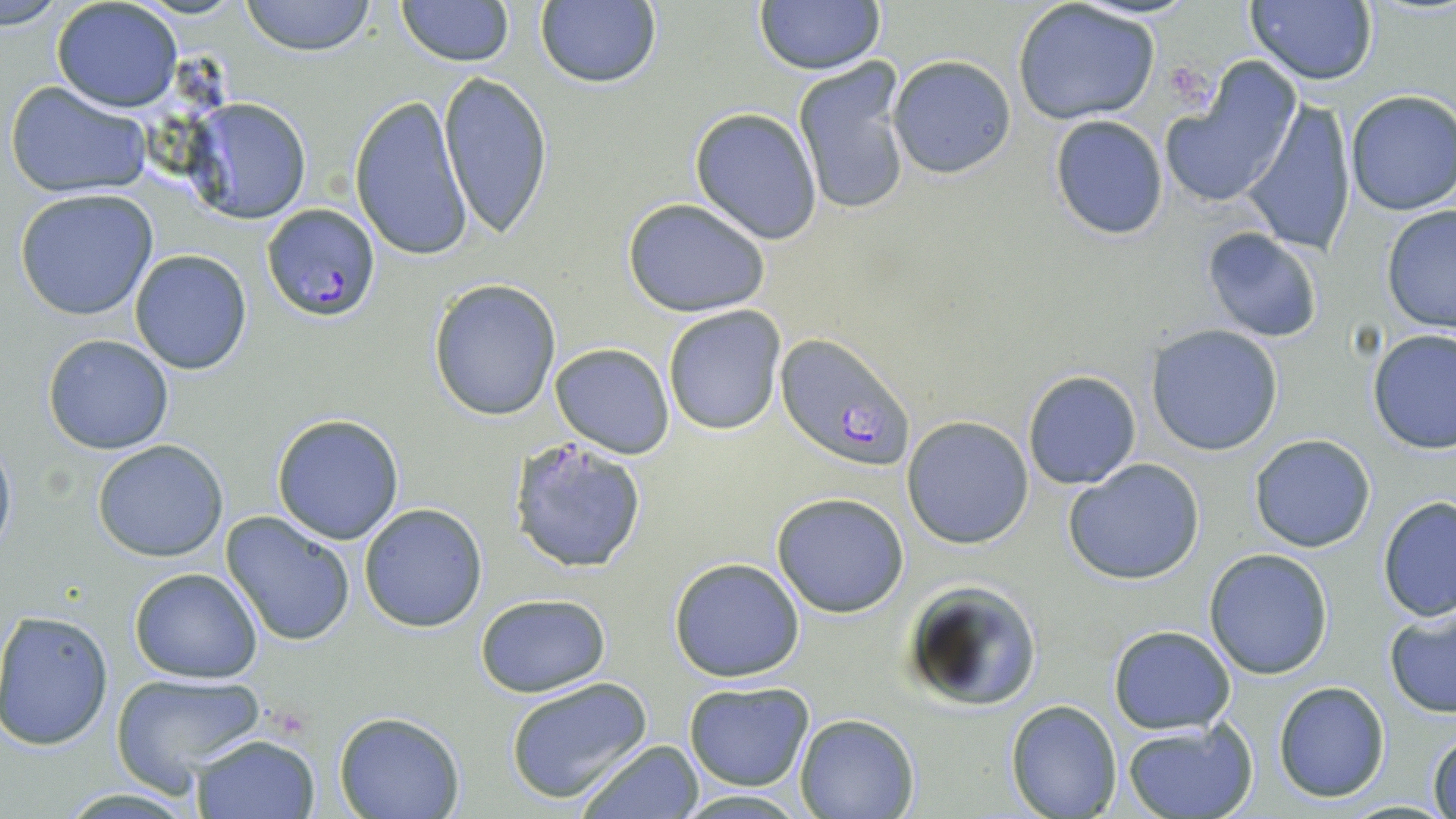

Approximate bounding boxes as (x1,y1)-(x2,y2) corner pairs in pixels. Plasmodium falciparum-infected red blood cell locations: (261,203)-(382,321), (775,335)-(915,474). Uninfected red blood cell locations: (239,0)-(379,56), (396,0)-(512,66), (3,1)-(61,29), (51,1)-(183,112), (534,1)-(663,89), (754,1)-(886,76), (1244,1)-(1380,89), (1013,2)-(1161,125), (887,54)-(1017,180), (792,60)-(911,217), (1160,68)-(1300,209), (438,70)-(554,238), (4,80)-(152,200), (1344,91)-(1456,215), (350,96)-(474,262), (181,98)-(312,224), (1242,101)-(1358,256), (690,108)-(821,245), (1048,116)-(1170,239), (15,189)-(159,321), (623,198)-(772,317), (1381,204)-(1456,334), (1200,227)-(1324,343), (129,249)-(253,375), (428,279)-(561,421), (661,304)-(786,435), (1147,326)-(1283,455), (1368,328)-(1456,455), (43,334)-(174,455), (550,343)-(673,459), (1022,369)-(1143,490), (272,413)-(406,543), (901,417)-(1034,549), (0,433)-(16,563), (1249,434)-(1377,553), (510,437)-(647,574), (92,439)-(229,562), (1064,458)-(1206,585), (771,492)-(910,618), (1377,495)-(1456,623), (359,503)-(489,634), (220,511)-(356,648), (1204,549)-(1334,679), (669,556)-(805,682), (129,567)-(263,682), (901,579)-(1042,712), (474,592)-(611,697), (1383,606)-(1456,720), (0,610)-(114,750), (1107,625)-(1236,733), (110,672)-(265,788), (504,676)-(653,804), (683,680)-(815,791), (1273,681)-(1389,803), (1006,699)-(1121,818), (332,712)-(466,819), (794,713)-(921,819), (1122,721)-(1257,819), (1428,730)-(1456,818), (190,732)-(322,819), (574,738)-(705,818), (673,789)-(811,818). Platelet locations: (1166,63)-(1223,113). Slide-level diagnosis: Plasmodium falciparum. Single field of view. Captured at 1000x magnification. Thin blood smear. Light microscopy. May-Grünwald-Giemsa stain. Image is 1456×819 pixels.